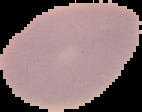

The area outside the segmented cell region is set to black. From a thin blood film. Image is 142×112 pixels. Result: no malaria parasites seen.